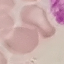

result = no malaria parasites detected
preparation = thin blood smear
capture = smartphone camera at the microscope eyepiece
image type = cell patch, automatically extracted from a larger field of view and resized to 64 × 64 pixels
stain = Giemsa